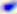

identification = Toxoplasma gondii
magnification = 400x
modality = micrograph